Locate every blood parasite and identify its species.
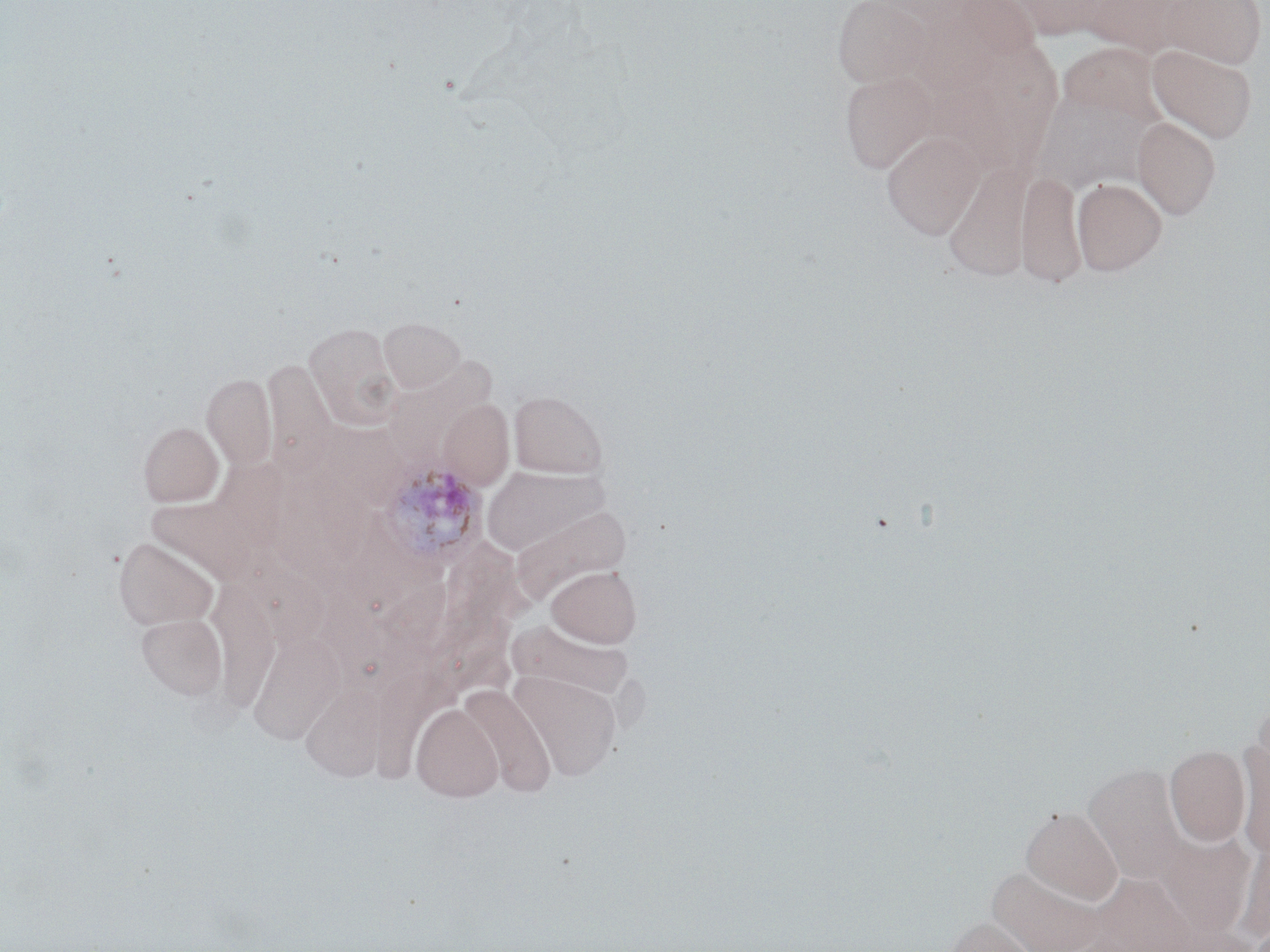

Approximate bounding boxes as (x1, y1, x2, y2) in pixels.
Plasmodium ovale-infected red blood cells: (378, 462, 487, 569).
No Plasmodium falciparum, Plasmodium malariae, Plasmodium vivax, Babesia divergens, or Trypanosoma brucei observed.

Uninfected red blood cell locations: (833, 0, 935, 87), (959, 0, 1044, 60), (1007, 0, 1111, 38), (1084, 0, 1190, 57), (1160, 0, 1266, 69), (1064, 43, 1178, 127), (1147, 44, 1257, 144), (839, 70, 939, 174), (1047, 94, 1150, 197), (1133, 116, 1221, 219), (882, 130, 984, 240), (943, 160, 1036, 282), (1017, 169, 1085, 287), (1072, 178, 1166, 275), (379, 317, 465, 393), (304, 322, 402, 431), (263, 358, 337, 472), (383, 358, 497, 465), (201, 373, 277, 470), (509, 391, 608, 478), (439, 399, 513, 489), (323, 418, 404, 510), (139, 421, 224, 506), (212, 456, 293, 551), (481, 466, 614, 560), (149, 498, 258, 584), (113, 536, 219, 630), (441, 537, 540, 642), (249, 546, 337, 651), (547, 566, 641, 647), (206, 580, 278, 722), (374, 580, 455, 661), (318, 597, 398, 687), (137, 613, 226, 699), (505, 618, 637, 707), (247, 629, 343, 745), (374, 669, 470, 791), (510, 670, 622, 780), (458, 684, 556, 796), (304, 685, 399, 782), (412, 703, 503, 801), (1235, 742, 1270, 860), (1164, 745, 1251, 847), (1083, 763, 1188, 885), (1021, 806, 1123, 905), (1159, 833, 1256, 937), (1237, 842, 1270, 944), (987, 865, 1106, 952), (942, 917, 1038, 952). Slide-level diagnosis: Plasmodium ovale. Thin blood film. Captured at 1000x magnification. Light microscopy. Single field of view. Image is 1270×952 pixels. May-Grünwald-Giemsa stain.